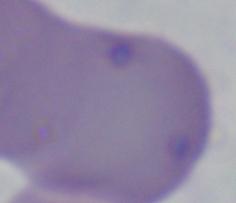
{
  "modality": "micrograph",
  "identification": "Babesia",
  "magnification": "1000x"
}